Classify this cell by malaria status.
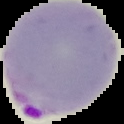
It is parasitized.

{
  "preparation": "thin blood smear",
  "image_type": "cell region segmented out of the field of view; surrounding area masked to black",
  "image_size": "124×124 pixels"
}